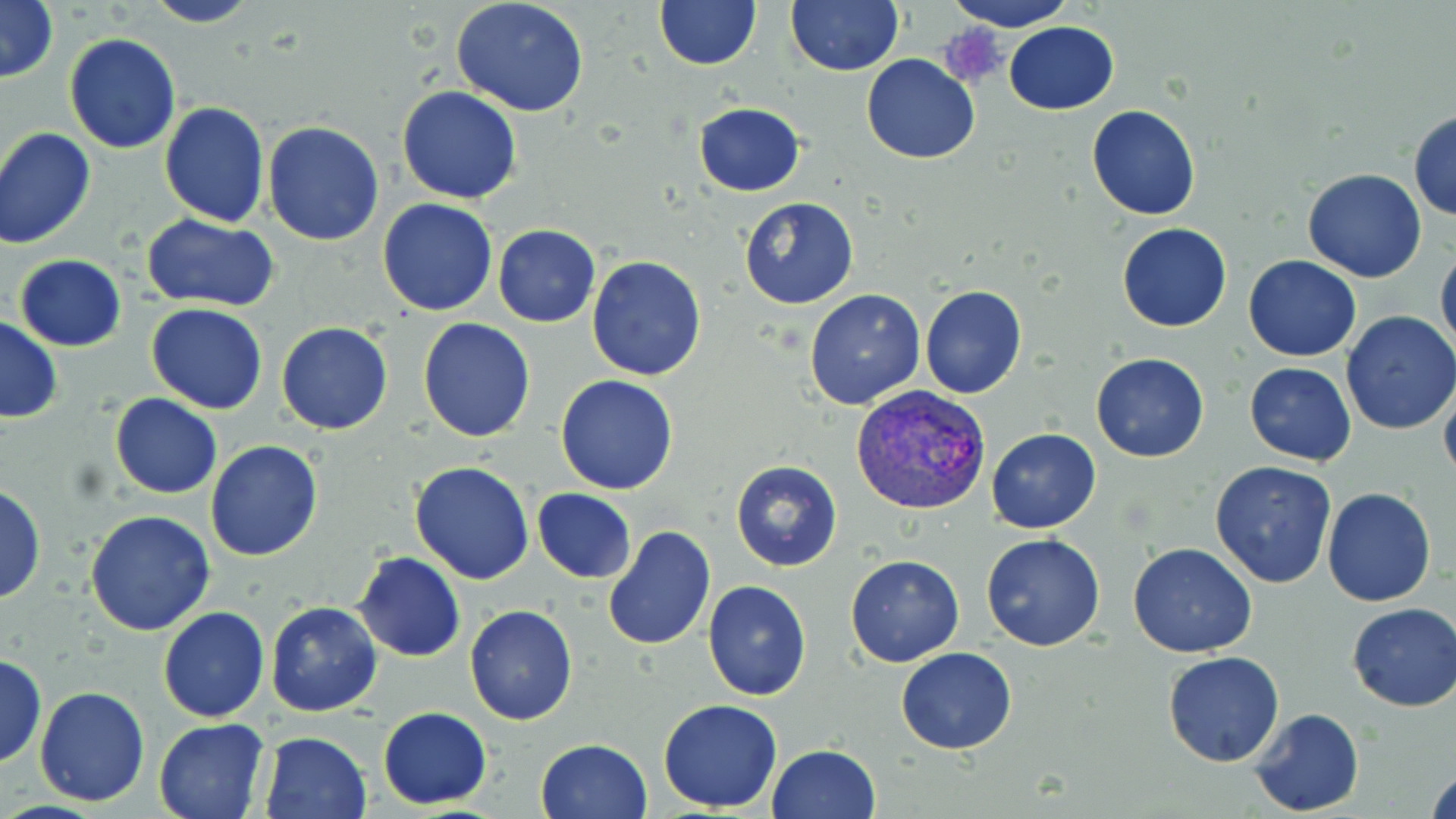

Summary:
  - Coordinate format: approximate bounding boxes as named x1/y1/x2/y2 corners in pixels
  - Plasmodium vivax-infected red blood cell locations: (x1=850, y1=384, x2=990, y2=515)
  - Uninfected red blood cell locations: (x1=0, y1=0, x2=57, y2=85), (x1=143, y1=0, x2=262, y2=27), (x1=450, y1=0, x2=591, y2=117), (x1=653, y1=0, x2=762, y2=71), (x1=787, y1=0, x2=903, y2=75), (x1=949, y1=0, x2=1073, y2=31), (x1=1004, y1=21, x2=1119, y2=114), (x1=64, y1=33, x2=181, y2=154), (x1=861, y1=53, x2=981, y2=164), (x1=397, y1=84, x2=523, y2=203), (x1=159, y1=102, x2=269, y2=228), (x1=693, y1=102, x2=806, y2=197), (x1=1086, y1=104, x2=1200, y2=219), (x1=1408, y1=109, x2=1456, y2=222), (x1=262, y1=121, x2=383, y2=247), (x1=0, y1=128, x2=96, y2=249), (x1=1302, y1=168, x2=1427, y2=283), (x1=738, y1=196, x2=858, y2=309), (x1=376, y1=199, x2=498, y2=316), (x1=139, y1=214, x2=280, y2=310), (x1=493, y1=224, x2=600, y2=328), (x1=1116, y1=224, x2=1233, y2=332), (x1=1435, y1=244, x2=1456, y2=358), (x1=14, y1=254, x2=126, y2=351), (x1=587, y1=255, x2=707, y2=380), (x1=1244, y1=255, x2=1362, y2=361), (x1=920, y1=285, x2=1027, y2=400), (x1=803, y1=289, x2=926, y2=410), (x1=146, y1=303, x2=269, y2=415), (x1=1341, y1=311, x2=1456, y2=434), (x1=0, y1=317, x2=63, y2=423), (x1=418, y1=317, x2=535, y2=440), (x1=277, y1=322, x2=393, y2=435), (x1=1090, y1=353, x2=1209, y2=463), (x1=1245, y1=363, x2=1357, y2=466), (x1=555, y1=375, x2=679, y2=495), (x1=1439, y1=375, x2=1456, y2=486), (x1=109, y1=393, x2=222, y2=498), (x1=985, y1=428, x2=1101, y2=534), (x1=205, y1=440, x2=323, y2=562), (x1=729, y1=460, x2=842, y2=571), (x1=409, y1=461, x2=535, y2=584), (x1=1209, y1=461, x2=1337, y2=589), (x1=0, y1=484, x2=45, y2=606), (x1=533, y1=487, x2=637, y2=583), (x1=1322, y1=487, x2=1436, y2=607), (x1=85, y1=510, x2=216, y2=636), (x1=604, y1=525, x2=715, y2=652), (x1=981, y1=534, x2=1105, y2=652), (x1=1128, y1=543, x2=1259, y2=658), (x1=353, y1=552, x2=465, y2=661), (x1=844, y1=554, x2=965, y2=667), (x1=703, y1=581, x2=812, y2=701), (x1=265, y1=600, x2=382, y2=717), (x1=1347, y1=603, x2=1456, y2=712), (x1=464, y1=605, x2=578, y2=726), (x1=156, y1=607, x2=270, y2=724), (x1=895, y1=647, x2=1018, y2=754), (x1=1163, y1=651, x2=1286, y2=767), (x1=0, y1=653, x2=47, y2=769), (x1=34, y1=685, x2=151, y2=806), (x1=658, y1=699, x2=783, y2=812), (x1=378, y1=707, x2=490, y2=809), (x1=1248, y1=708, x2=1364, y2=816), (x1=153, y1=717, x2=270, y2=819), (x1=258, y1=730, x2=371, y2=817), (x1=535, y1=738, x2=653, y2=819), (x1=766, y1=745, x2=880, y2=819), (x1=1426, y1=762, x2=1455, y2=818)
  - Platelet locations: (x1=940, y1=25, x2=1009, y2=91)
  - Slide-level diagnosis: Plasmodium vivax
  - Image size: 1456×819 pixels
  - Magnification: 1000x
  - Field of view: one of a larger specimen
  - Stain: May-Grünwald-Giemsa
  - Modality: light microscopy
  - Preparation: thin blood smear